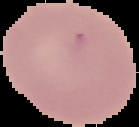

Cell region segmented out of the field of view; the surrounding area is masked to black. Malaria status: uninfected. From a thin blood film. Image is 139×127 pixels.